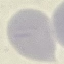 Malaria status: uninfected. Automatically extracted cell patch, resized to 64 × 64 pixels. Giemsa-stained preparation. Acquired by smartphone through the microscope eyepiece. Thin blood smear.